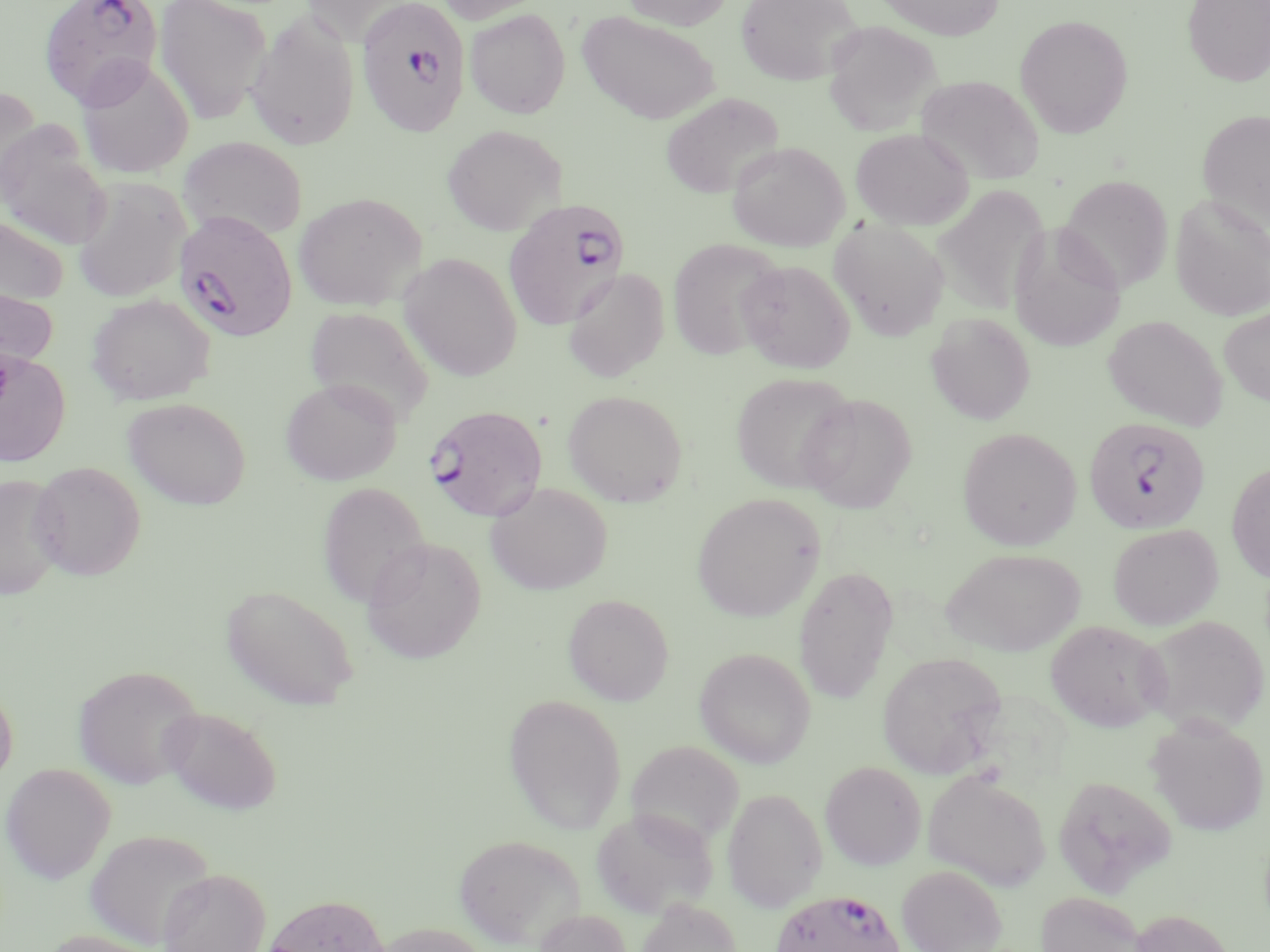 Approximate bounding boxes as [x1, y1, x2, y2] in pixels. Plasmodium falciparum-infected red blood cell locations: [38, 0, 165, 108], [357, 0, 471, 138], [503, 198, 632, 335], [177, 212, 301, 342], [424, 404, 548, 522], [1083, 417, 1210, 535], [771, 888, 905, 952]. Uninfected red blood cell locations: [154, 0, 272, 124], [298, 0, 418, 45], [435, 0, 552, 24], [621, 0, 733, 30], [735, 0, 862, 85], [876, 0, 1005, 40], [1183, 0, 1270, 86], [465, 8, 571, 119], [245, 11, 360, 152], [577, 11, 719, 125], [1015, 13, 1133, 137], [823, 21, 941, 135], [75, 58, 194, 179], [915, 75, 1045, 185], [0, 88, 42, 204], [660, 93, 783, 199], [1197, 109, 1270, 229], [0, 122, 111, 249], [442, 124, 565, 236], [851, 128, 973, 230], [177, 136, 307, 240], [727, 141, 849, 252], [1058, 174, 1173, 293], [73, 177, 192, 302], [933, 185, 1049, 315], [293, 192, 427, 311], [1170, 194, 1269, 321], [0, 215, 69, 307], [829, 219, 950, 341], [1008, 224, 1126, 353], [667, 238, 785, 360], [399, 252, 522, 382], [736, 259, 855, 373], [563, 268, 670, 383], [0, 282, 58, 378], [86, 293, 216, 405], [304, 306, 434, 425], [1219, 306, 1270, 406], [926, 312, 1036, 424], [1103, 315, 1228, 430], [0, 350, 70, 466], [730, 372, 857, 493], [281, 377, 401, 485], [562, 389, 688, 507], [798, 393, 918, 513], [123, 397, 251, 510], [957, 426, 1081, 550], [30, 461, 146, 581], [1226, 461, 1270, 583], [0, 474, 67, 598], [317, 481, 431, 609], [485, 482, 613, 595], [691, 493, 824, 622], [1108, 523, 1223, 630], [361, 537, 486, 664], [943, 548, 1085, 656], [793, 565, 900, 704], [221, 584, 359, 710], [563, 594, 674, 706], [1140, 614, 1269, 736], [1046, 620, 1171, 732], [694, 647, 815, 768], [877, 652, 1008, 778], [73, 664, 204, 789], [0, 682, 18, 786], [504, 693, 627, 835], [160, 706, 282, 815], [1146, 717, 1268, 836], [627, 740, 745, 850], [820, 761, 926, 870], [1, 762, 116, 883], [922, 770, 1051, 891], [1053, 775, 1176, 898], [722, 788, 827, 912], [590, 806, 717, 919], [84, 828, 216, 948], [452, 833, 585, 948], [897, 864, 1007, 952], [158, 867, 271, 952], [1035, 890, 1147, 952], [261, 893, 390, 952], [637, 898, 741, 952], [532, 909, 633, 952], [1129, 909, 1238, 952], [371, 921, 491, 952], [38, 930, 164, 952]. Slide-level diagnosis: Plasmodium falciparum. May-Grünwald-Giemsa-stained preparation. Thin blood smear. Single field of view. Image is 1270×952 pixels. Captured at 1000x magnification. Optical microscopy.